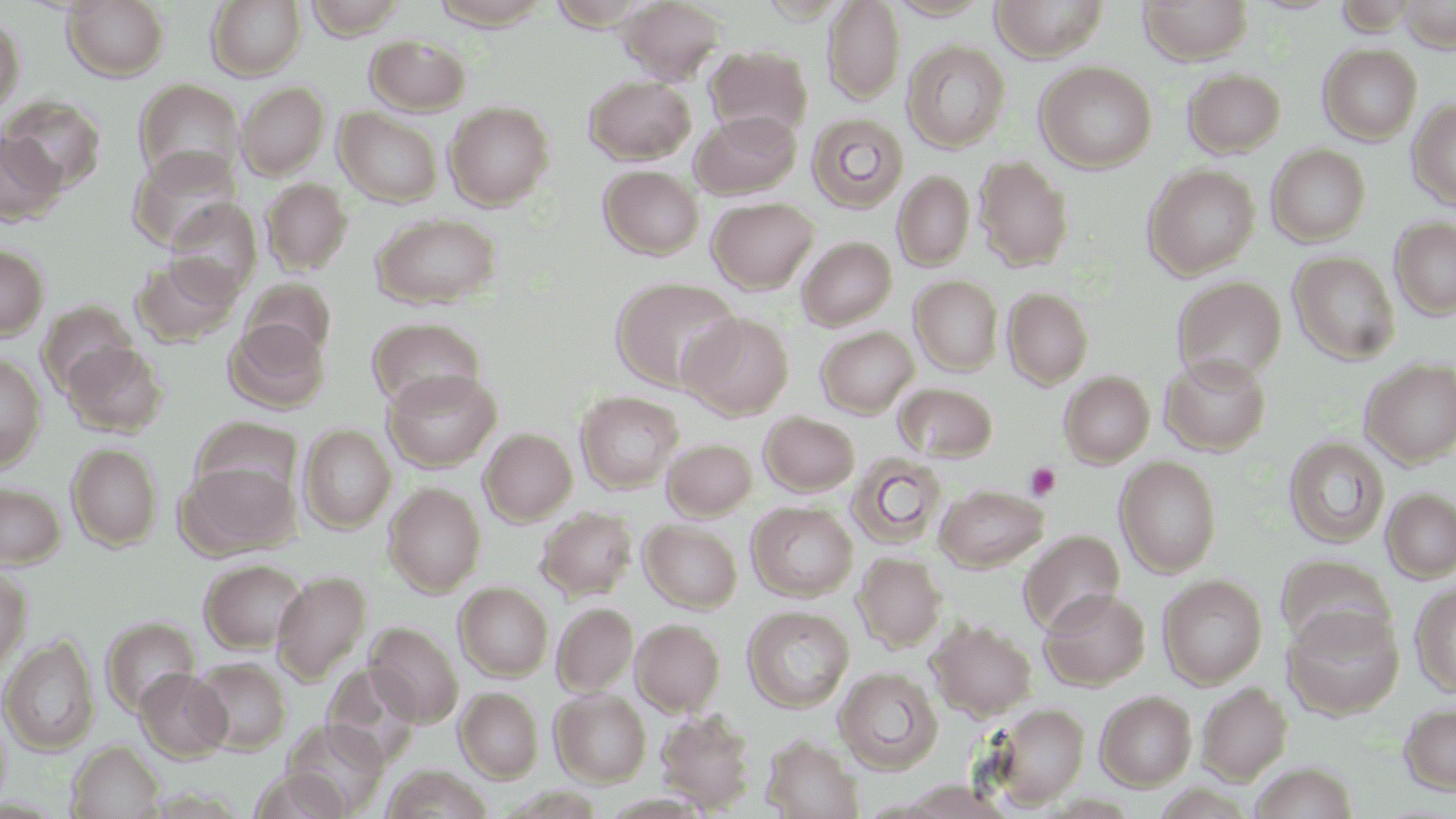

Summary:
  - Coordinate format: approximate bounding boxes as [x1, y1, x2, y2] in pixels
  - Platelet locations: [1025, 462, 1061, 501]
  - Uninfected red blood cell locations: [62, 0, 169, 81], [207, 0, 306, 80], [305, 0, 410, 40], [885, 0, 992, 20], [990, 0, 1109, 61], [1139, 0, 1253, 64], [1398, 0, 1455, 52], [617, 1, 725, 85], [823, 1, 905, 104], [0, 16, 25, 116], [365, 34, 472, 115], [903, 40, 1010, 152], [1318, 43, 1422, 144], [705, 45, 813, 139], [1035, 61, 1157, 172], [1183, 68, 1286, 157], [584, 75, 697, 164], [132, 79, 245, 185], [237, 81, 331, 179], [1, 95, 106, 193], [1408, 99, 1456, 210], [444, 101, 555, 210], [335, 107, 443, 207], [690, 110, 803, 199], [807, 113, 909, 213], [0, 131, 65, 226], [1266, 145, 1370, 246], [130, 146, 243, 251], [973, 155, 1074, 270], [1143, 164, 1260, 278], [598, 165, 704, 259], [893, 170, 975, 271], [260, 178, 353, 275], [707, 197, 818, 293], [164, 198, 261, 300], [371, 213, 501, 310], [1391, 218, 1456, 319], [797, 236, 896, 330], [0, 244, 48, 339], [1289, 252, 1401, 364], [131, 254, 240, 348], [910, 276, 1003, 375], [1172, 276, 1287, 383], [610, 277, 743, 392], [241, 278, 336, 362], [1003, 287, 1093, 388], [681, 312, 795, 419], [367, 317, 487, 412], [224, 318, 330, 413], [815, 326, 919, 417], [61, 341, 167, 437], [1160, 353, 1271, 454], [0, 354, 46, 472], [1360, 358, 1456, 467], [382, 368, 502, 472], [1059, 371, 1155, 467], [895, 383, 997, 461], [575, 391, 684, 493], [759, 411, 860, 495], [191, 418, 302, 505], [299, 424, 396, 533], [480, 428, 577, 526], [1284, 436, 1390, 547], [663, 438, 758, 520], [67, 443, 162, 550], [846, 452, 947, 549], [1115, 455, 1222, 577], [182, 460, 298, 556], [0, 481, 66, 567], [384, 482, 486, 596], [934, 483, 1049, 572], [1382, 488, 1456, 583], [747, 501, 858, 601], [537, 507, 638, 600], [640, 520, 743, 612], [1018, 530, 1125, 635], [852, 551, 947, 651], [1276, 554, 1395, 652], [199, 558, 309, 653], [0, 566, 31, 673], [272, 571, 371, 683], [1158, 574, 1268, 688], [455, 582, 553, 681], [1411, 583, 1456, 697], [1039, 587, 1150, 690], [552, 603, 639, 696], [1282, 604, 1403, 719], [742, 605, 855, 713], [101, 617, 200, 717], [631, 618, 725, 715], [927, 618, 1037, 720], [366, 621, 464, 727], [1, 635, 99, 755], [190, 657, 291, 754], [323, 663, 422, 768], [835, 667, 944, 774], [135, 668, 231, 762], [1196, 681, 1292, 783], [455, 687, 543, 783], [550, 689, 651, 787], [1095, 690, 1197, 790], [1399, 701, 1456, 795], [990, 702, 1090, 808], [655, 707, 757, 813], [0, 709, 12, 810], [281, 720, 389, 816], [761, 734, 864, 818], [67, 741, 164, 819], [1250, 762, 1358, 819], [381, 765, 495, 818]
  - Slide-level diagnosis: negative for blood parasites
  - Stain: May-Grünwald-Giemsa
  - Preparation: thin blood smear
  - Field of view: one of a larger specimen
  - Image size: 1456×819 pixels
  - Magnification: 1000x
  - Modality: optical microscopy